Locate every uninfected red blood cell.
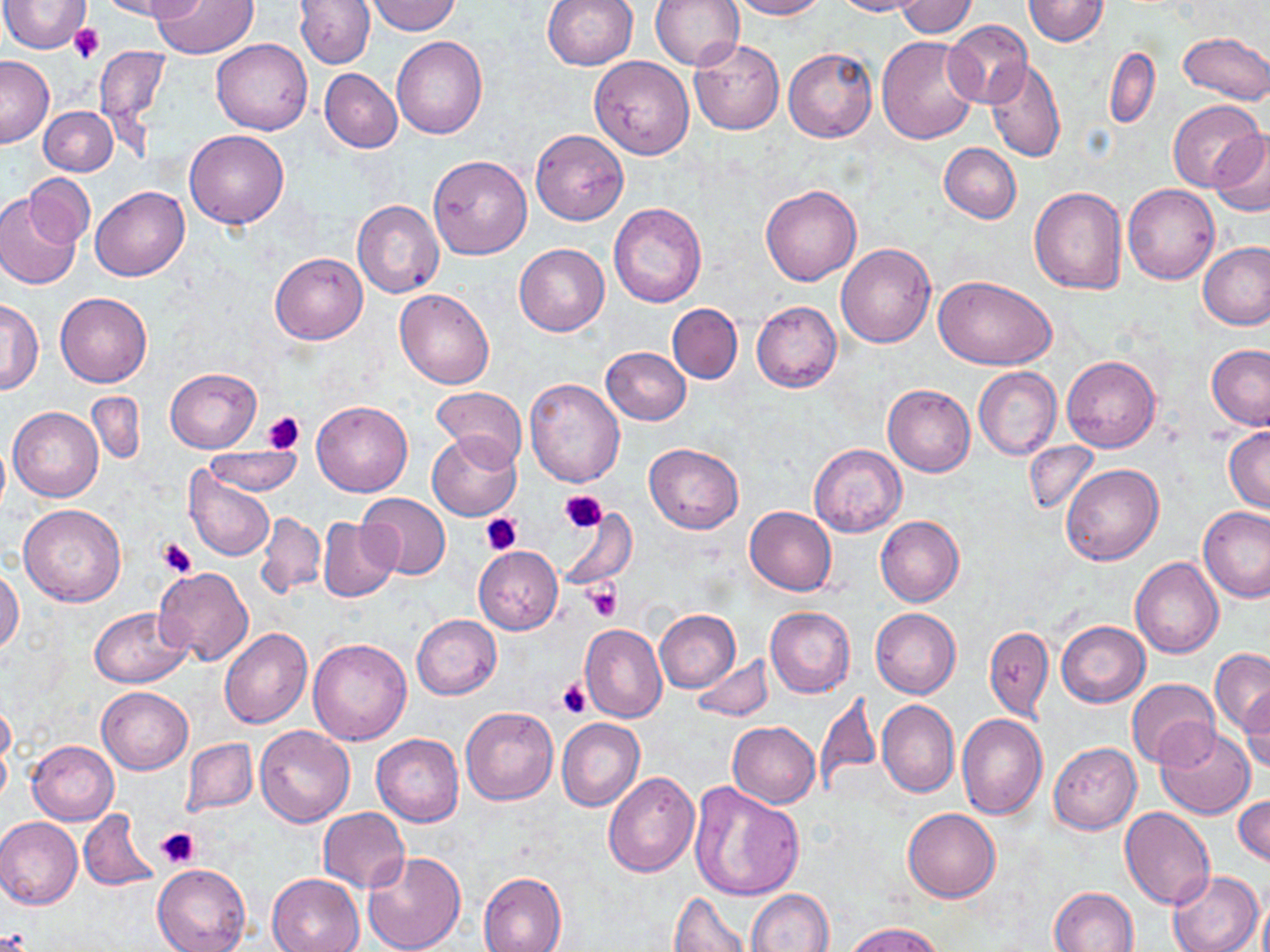

Approximate bounding boxes as (x1,y1)-(x2,y2) corner pairs in pixels.
Uninfected red blood cells: (0,0)-(90,53), (97,0)-(201,21), (295,0)-(375,68), (542,0)-(638,70), (650,0)-(743,71), (727,0)-(828,19), (834,0)-(926,16), (896,0)-(977,38), (1022,0)-(1110,45), (152,1)-(258,58), (366,1)-(461,35), (64,21)-(108,65), (943,21)-(1032,110), (1178,31)-(1270,106), (392,36)-(487,138), (876,36)-(978,143), (211,38)-(313,135), (689,40)-(784,135), (1105,46)-(1160,129), (94,47)-(168,131), (784,48)-(877,142), (0,55)-(53,147), (589,56)-(694,158), (984,58)-(1066,161), (320,69)-(402,153), (1168,100)-(1264,192), (40,105)-(117,176), (1210,129)-(1270,217), (184,130)-(290,229), (531,130)-(628,225), (939,143)-(1021,223), (428,155)-(532,259), (25,174)-(94,250), (760,184)-(862,286), (1123,184)-(1219,284), (91,185)-(189,281), (1029,187)-(1126,294), (1,195)-(80,290), (353,201)-(445,299), (609,202)-(707,309), (1200,242)-(1270,330), (514,243)-(609,337), (836,243)-(935,348), (271,252)-(367,343), (935,275)-(1056,369), (395,288)-(494,389), (55,292)-(152,387), (1,298)-(43,393), (752,301)-(841,392), (668,304)-(742,384), (1207,344)-(1270,430), (601,347)-(691,424), (1062,356)-(1160,452), (973,367)-(1061,459), (165,368)-(260,452), (886,376)-(1061,464), (525,377)-(625,488), (883,384)-(974,476), (431,386)-(529,467), (85,391)-(145,467), (311,398)-(413,497), (8,406)-(103,501), (1224,427)-(1269,512), (428,432)-(521,520), (0,440)-(10,516), (1024,440)-(1099,516), (644,442)-(744,533), (809,443)-(906,536), (204,446)-(303,497), (1061,463)-(1163,565), (184,465)-(275,563), (360,493)-(450,579), (17,503)-(126,605), (1199,505)-(1270,603), (745,506)-(836,595), (559,508)-(636,589), (256,512)-(325,597), (875,516)-(965,606), (318,518)-(399,602), (473,546)-(563,634), (1131,557)-(1224,658), (153,566)-(253,666), (0,569)-(23,653), (89,606)-(192,687), (765,606)-(855,697), (871,608)-(961,699), (654,609)-(740,691), (411,614)-(501,699), (1057,620)-(1150,706), (579,622)-(667,722), (984,625)-(1054,721), (219,628)-(312,728), (308,638)-(412,746), (1210,648)-(1270,735), (690,656)-(774,723), (1125,677)-(1221,769), (96,687)-(193,773), (1239,688)-(1269,772), (814,691)-(881,801), (0,697)-(15,772), (877,699)-(958,798), (461,707)-(559,805), (957,713)-(1048,818), (557,718)-(644,812), (727,721)-(821,808), (254,726)-(355,827), (1155,727)-(1255,819), (371,734)-(463,827), (182,737)-(257,816), (28,740)-(118,824), (1049,742)-(1141,834), (604,772)-(699,877), (689,782)-(805,901), (1234,794)-(1270,868), (318,807)-(409,892), (1120,807)-(1216,912), (903,808)-(1001,902), (78,811)-(158,891), (1,816)-(83,909), (361,851)-(466,952), (152,864)-(250,951), (1167,870)-(1264,952), (478,872)-(566,952), (266,873)-(363,952), (1051,886)-(1140,952), (746,888)-(834,952), (670,889)-(752,952), (847,922)-(948,952).

Summary:
  - Platelet locations: (71,23)-(104,64), (261,410)-(305,455), (558,492)-(605,536), (480,514)-(522,555), (158,537)-(198,579), (583,581)-(624,621), (557,677)-(593,718), (157,826)-(201,870), (0,929)-(32,950)
  - Slide-level diagnosis: negative for blood parasites
  - Field of view: single
  - Modality: optical microscopy
  - Preparation: thin blood smear
  - Stain: May-Grünwald-Giemsa
  - Magnification: 1000x
  - Image size: 1270×952 pixels